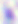
identification = Toxoplasma gondii
magnification = 400x
modality = micrograph